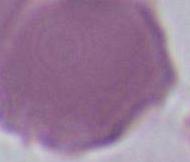 Captured at 1000x magnification. Photomicrograph. A red blood cell is seen.